Identify the parasite.
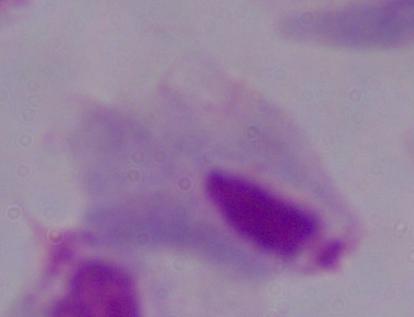
This is a trichomonad.

Photomicrograph. 1000x magnification.